Locate every leukocyte (white blood cell).
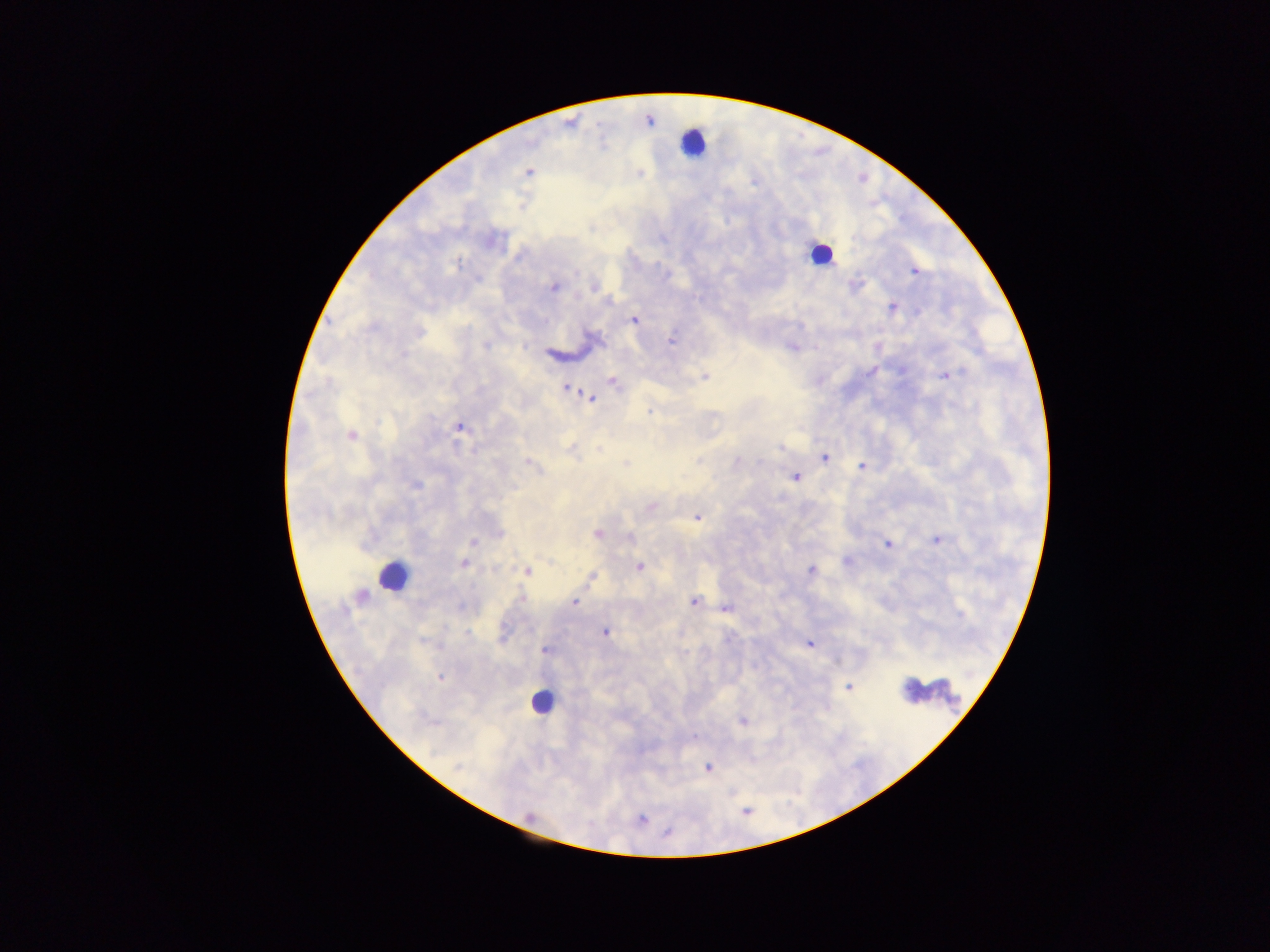

Approximate centers as (x, y) in pixels.
Leukocytes: (693, 143), (821, 253), (391, 576), (931, 694), (541, 701).

image size = 1270×952 pixels
country = Ghana
capture = mobile-phone photograph through a microscope
field of view = single
preparation = thick blood smear
malaria parasite locations = approximate centers as (x, y) in pixels: (528, 172), (915, 271), (593, 286), (554, 287), (893, 306), (634, 320), (672, 341), (792, 346), (945, 375), (704, 376), (612, 380), (566, 388), (589, 397), (460, 427), (350, 435), (780, 447), (572, 449), (825, 457), (529, 463), (862, 465), (795, 477), (414, 484), (650, 506), (696, 517), (597, 533), (937, 540), (473, 542), (886, 544), (463, 563), (639, 566), (811, 569), (527, 571), (591, 577), (574, 601), (694, 601), (727, 607), (605, 632), (809, 644), (545, 649), (440, 677), (849, 686), (743, 720), (709, 766), (641, 819)